Identify the parasite.
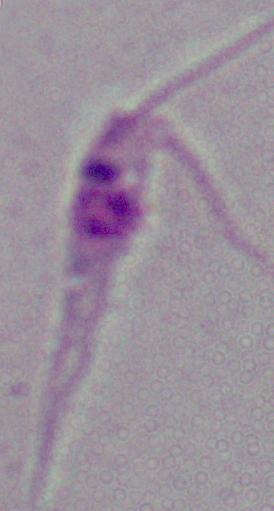

Leishmania.

Photomicrograph. Captured at 1000x magnification.